Locate every malaria parasite and every leukocyte.
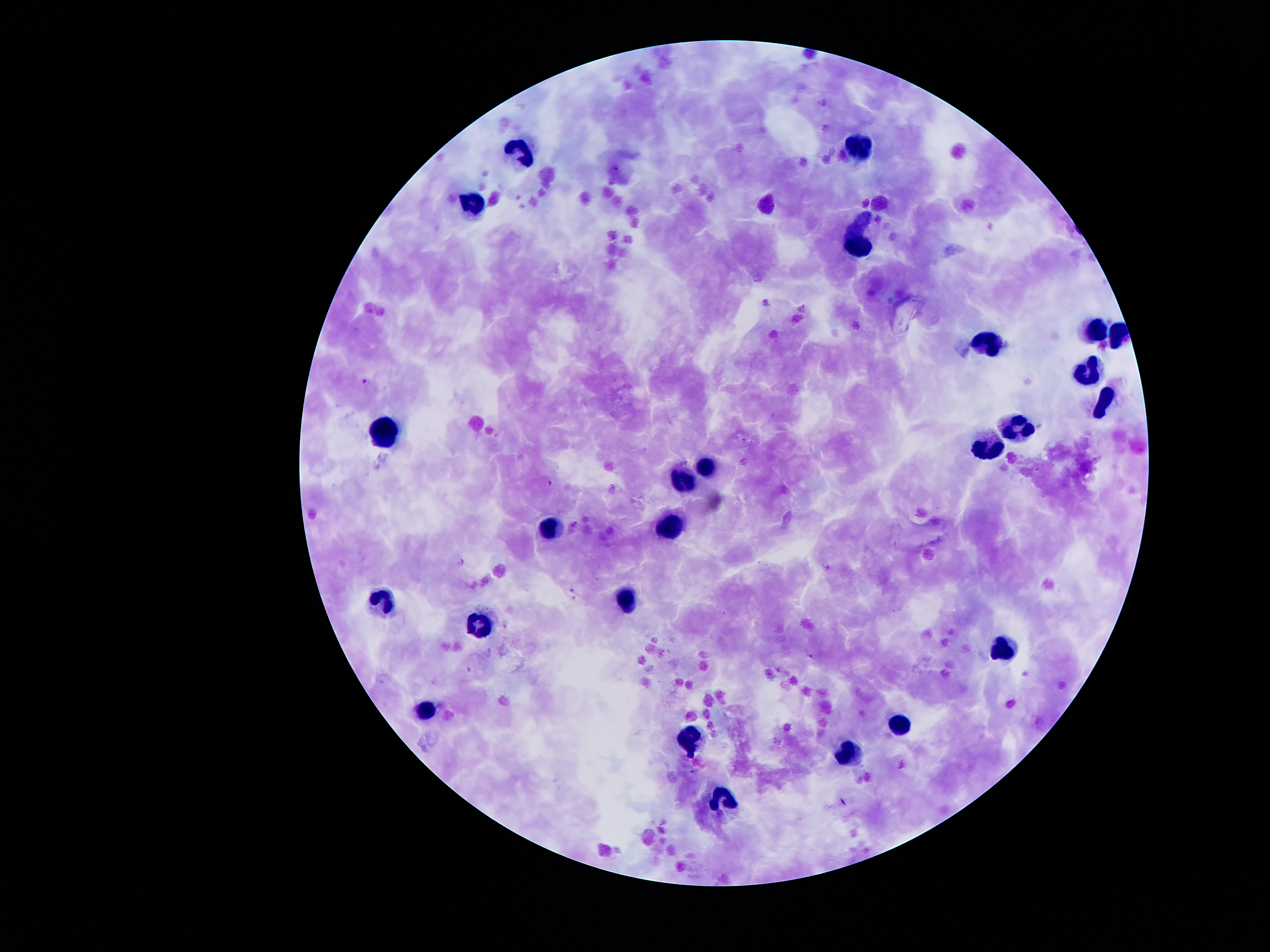
Approximate centers as (x, y) in pixels.
Malaria parasites: (617, 168), (366, 382), (550, 483), (463, 561), (812, 658), (844, 803).
Leukocytes: (858, 143), (523, 149), (462, 204), (854, 240), (1093, 330), (988, 339), (1084, 371), (1101, 403), (1013, 427), (382, 435), (987, 445), (708, 466), (677, 483), (669, 525), (552, 528), (626, 595), (388, 596), (478, 625), (1002, 649), (430, 714), (899, 722), (689, 734), (846, 754), (723, 797).

Summary:
  - Magnification: 100x
  - Image size: 1270×952 pixels
  - Capture: smartphone through the microscope eyepiece
  - Preparation: thick peripheral-blood smear
  - Field of view: single
  - Patient malaria status: positive for Plasmodium falciparum
  - Stain: Giemsa